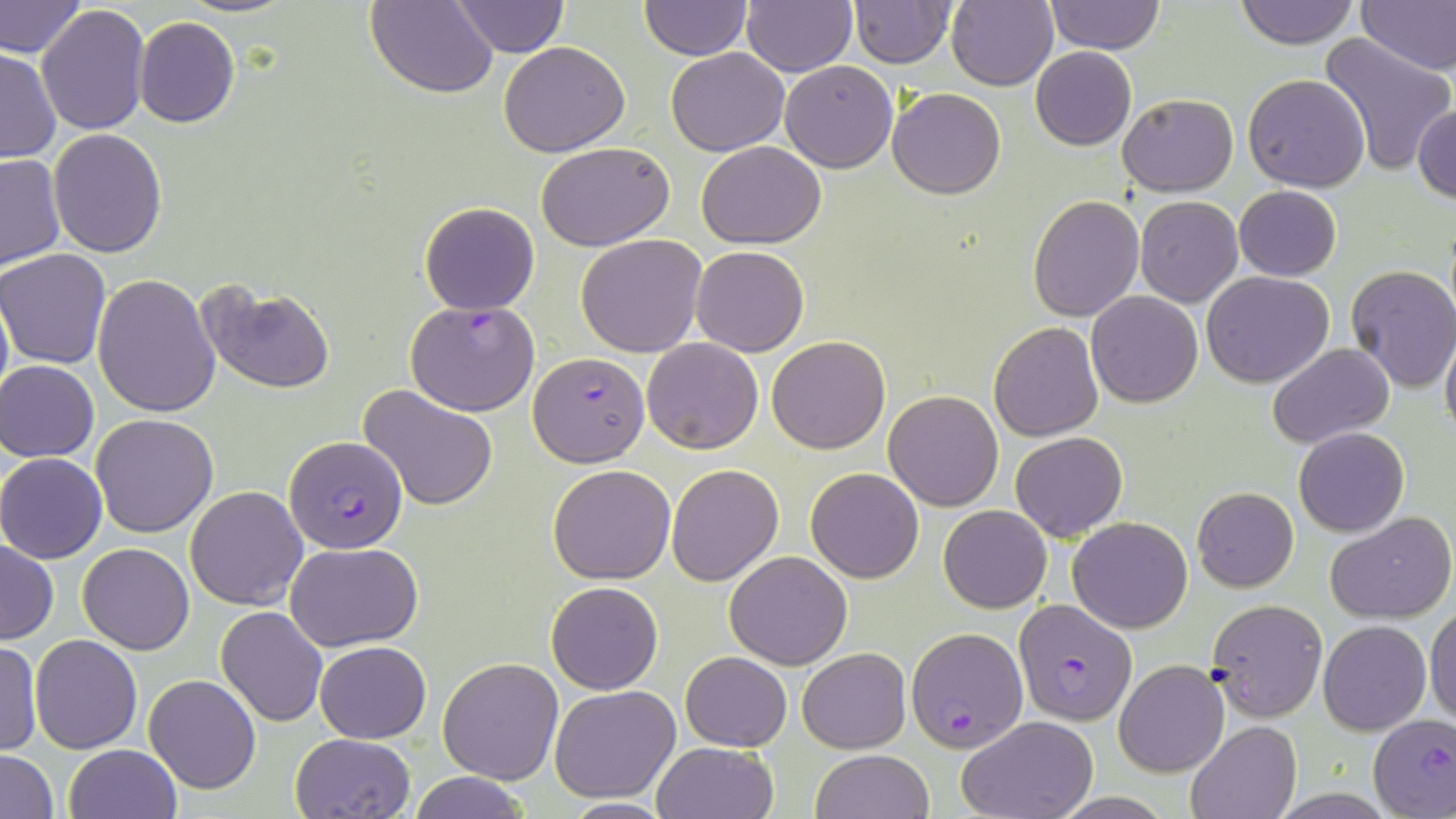

slide-level diagnosis = Plasmodium falciparum
image size = 1456×819 pixels
modality = optical microscopy
field of view = one of a larger specimen
uninfected red blood cell locations = approximate bounding boxes as named x1/y1/x2/y2 corners in pixels: (x1=1, y1=0, x2=85, y2=61), (x1=173, y1=0, x2=300, y2=18), (x1=366, y1=0, x2=498, y2=97), (x1=640, y1=0, x2=750, y2=58), (x1=1044, y1=0, x2=1164, y2=54), (x1=1234, y1=0, x2=1359, y2=48), (x1=1357, y1=0, x2=1456, y2=74), (x1=739, y1=1, x2=856, y2=76), (x1=946, y1=1, x2=1058, y2=89), (x1=451, y1=2, x2=568, y2=55), (x1=849, y1=2, x2=955, y2=68), (x1=37, y1=4, x2=151, y2=137), (x1=135, y1=16, x2=240, y2=128), (x1=1317, y1=34, x2=1454, y2=176), (x1=498, y1=40, x2=630, y2=158), (x1=1029, y1=46, x2=1136, y2=150), (x1=0, y1=48, x2=60, y2=164), (x1=666, y1=48, x2=788, y2=156), (x1=779, y1=60, x2=897, y2=170), (x1=1242, y1=74, x2=1370, y2=192), (x1=888, y1=87, x2=1005, y2=199), (x1=1118, y1=92, x2=1237, y2=196), (x1=1414, y1=103, x2=1455, y2=205), (x1=47, y1=129, x2=167, y2=258), (x1=696, y1=139, x2=827, y2=248), (x1=537, y1=141, x2=675, y2=249), (x1=0, y1=154, x2=65, y2=270), (x1=1233, y1=185, x2=1343, y2=280), (x1=1028, y1=195, x2=1143, y2=321), (x1=1135, y1=196, x2=1242, y2=307), (x1=419, y1=201, x2=541, y2=315), (x1=575, y1=234, x2=708, y2=357), (x1=691, y1=246, x2=809, y2=355), (x1=1, y1=249, x2=114, y2=367), (x1=1344, y1=265, x2=1456, y2=393), (x1=1201, y1=271, x2=1334, y2=388), (x1=92, y1=273, x2=220, y2=416), (x1=196, y1=281, x2=336, y2=393), (x1=0, y1=285, x2=12, y2=415), (x1=1086, y1=291, x2=1203, y2=407), (x1=989, y1=322, x2=1103, y2=440), (x1=1440, y1=327, x2=1456, y2=446), (x1=767, y1=336, x2=891, y2=454), (x1=641, y1=338, x2=763, y2=454), (x1=1268, y1=342, x2=1395, y2=450), (x1=1, y1=360, x2=100, y2=463), (x1=358, y1=384, x2=499, y2=511), (x1=883, y1=389, x2=1004, y2=511), (x1=91, y1=414, x2=218, y2=537), (x1=1293, y1=427, x2=1409, y2=537), (x1=1010, y1=430, x2=1128, y2=540), (x1=0, y1=453, x2=107, y2=563), (x1=665, y1=463, x2=784, y2=585), (x1=549, y1=464, x2=676, y2=584), (x1=806, y1=466, x2=925, y2=583), (x1=186, y1=485, x2=308, y2=609), (x1=1192, y1=486, x2=1299, y2=592), (x1=939, y1=504, x2=1051, y2=612), (x1=1325, y1=511, x2=1456, y2=624), (x1=1068, y1=517, x2=1192, y2=633), (x1=0, y1=539, x2=58, y2=644), (x1=78, y1=541, x2=195, y2=654), (x1=284, y1=543, x2=424, y2=651), (x1=723, y1=549, x2=853, y2=670), (x1=546, y1=581, x2=664, y2=694), (x1=1205, y1=599, x2=1328, y2=719), (x1=1426, y1=602, x2=1456, y2=726), (x1=216, y1=606, x2=328, y2=726), (x1=1318, y1=619, x2=1432, y2=736), (x1=31, y1=635, x2=142, y2=753), (x1=0, y1=639, x2=41, y2=755), (x1=315, y1=640, x2=432, y2=743), (x1=797, y1=648, x2=911, y2=752), (x1=679, y1=651, x2=792, y2=751), (x1=438, y1=657, x2=565, y2=783), (x1=1113, y1=660, x2=1229, y2=777), (x1=144, y1=674, x2=261, y2=795), (x1=549, y1=684, x2=681, y2=802), (x1=956, y1=715, x2=1099, y2=819), (x1=1186, y1=720, x2=1301, y2=819), (x1=290, y1=732, x2=414, y2=818), (x1=651, y1=741, x2=779, y2=819), (x1=62, y1=744, x2=180, y2=819), (x1=1, y1=750, x2=59, y2=819), (x1=810, y1=750, x2=933, y2=819), (x1=408, y1=771, x2=530, y2=819), (x1=550, y1=799, x2=681, y2=817)
stain = May-Grünwald-Giemsa
preparation = thin blood film
Plasmodium falciparum-infected red blood cell locations = approximate bounding boxes as named x1/y1/x2/y2 corners in pixels: (x1=405, y1=301, x2=540, y2=417), (x1=530, y1=351, x2=647, y2=465), (x1=285, y1=435, x2=409, y2=554), (x1=1015, y1=600, x2=1136, y2=725), (x1=908, y1=628, x2=1026, y2=753), (x1=1370, y1=715, x2=1455, y2=816)
magnification = 1000x